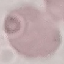

Result: no malaria parasites detected. Thin blood smear. Automatically extracted cell patch, resized to 64 × 64 pixels. Giemsa-stained preparation. Photographed with a smartphone camera at the microscope eyepiece.